Classify this cell by malaria status.
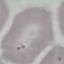
Uninfected.

Photographed with a smartphone camera at the microscope eyepiece. Thin blood smear. Automatically extracted cell patch, resized to 64 × 64 pixels. Giemsa-stained preparation.